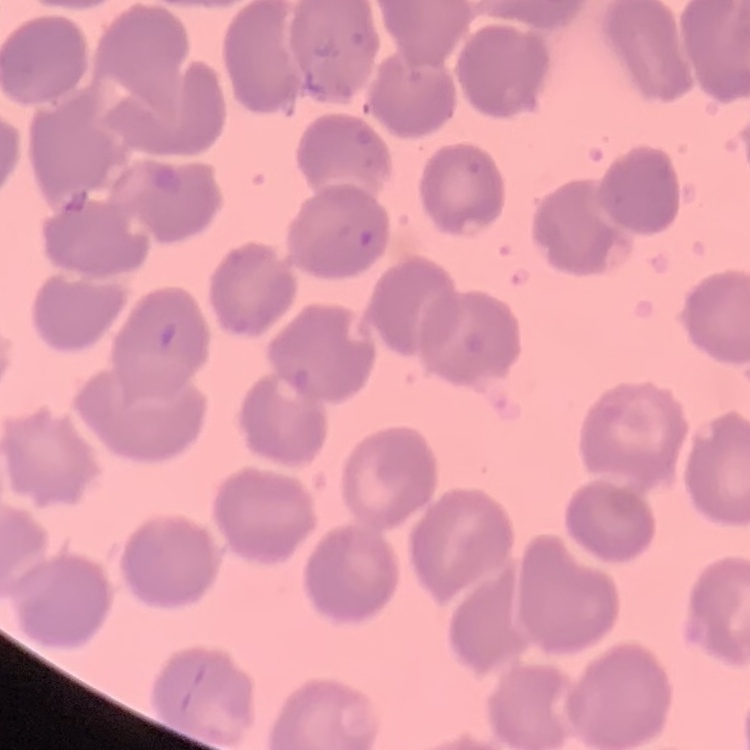
The erythrocytes exhibit no rouleaux formation. Stained with either Field's or Giemsa. Thin peripheral smear. Square crop of a larger photomicrograph.